Outline each blood parasite and name the species.
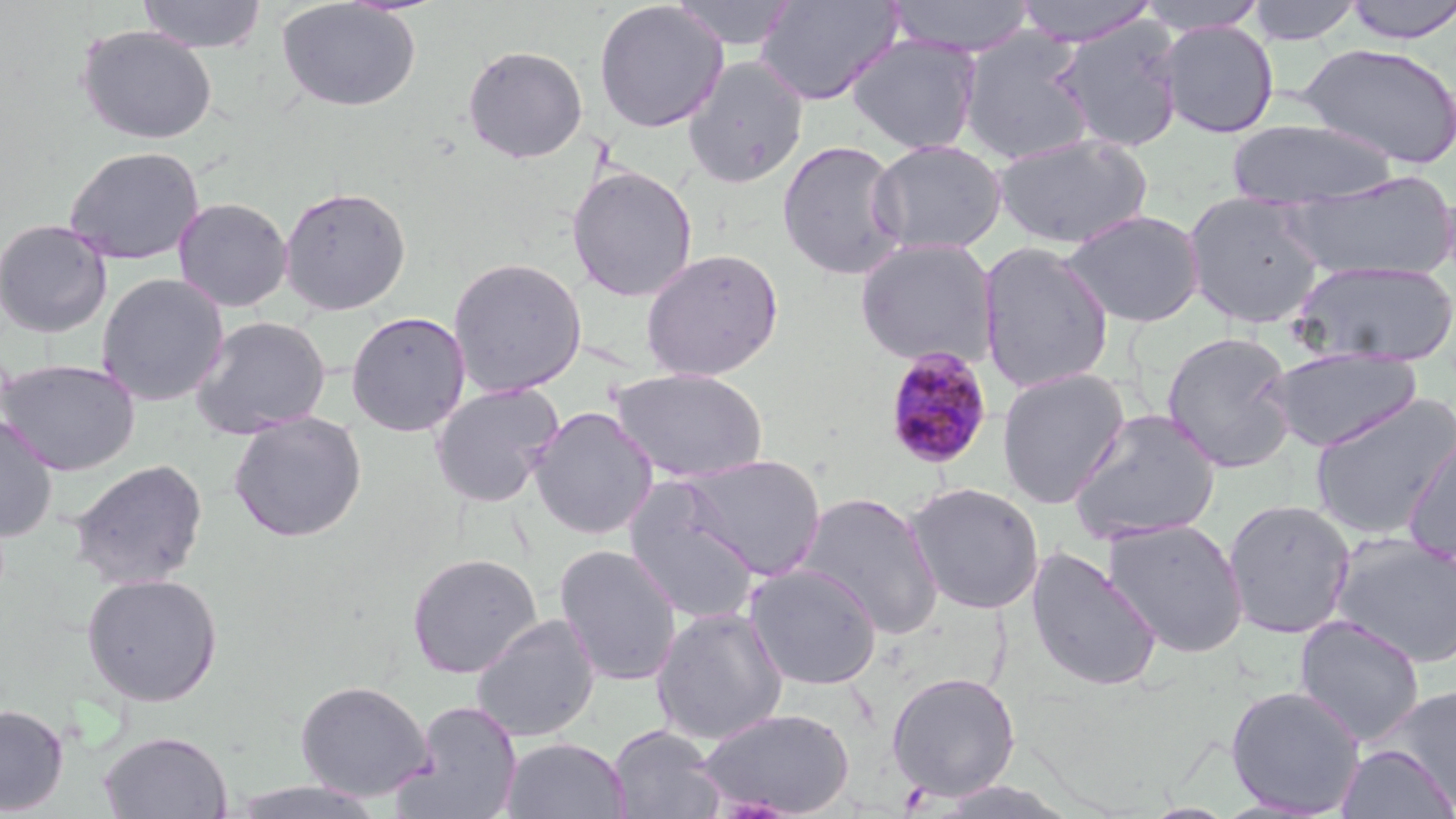
Approximate bounding boxes as (x1,y1)-(x2,y2) corner pairs in pixels.
Plasmodium malariae-infected red blood cells: (883,346)-(993,471).
No Plasmodium falciparum, Plasmodium ovale, Plasmodium vivax, Babesia divergens, or Trypanosoma brucei observed.

Summary:
  - Uninfected red blood cell locations: (136,0)-(267,54), (672,0)-(798,51), (886,0)-(1037,57), (1012,0)-(1159,46), (1342,0)-(1456,44), (593,1)-(728,133), (754,1)-(904,106), (1137,1)-(1269,35), (1244,1)-(1365,44), (276,2)-(422,113), (1051,17)-(1186,153), (1158,20)-(1279,139), (75,25)-(218,145), (958,30)-(1096,165), (845,34)-(984,155), (1298,41)-(1456,169), (462,44)-(589,163), (683,56)-(809,189), (1227,119)-(1397,208), (991,132)-(1154,250), (776,139)-(909,281), (869,139)-(1007,256), (63,145)-(205,265), (566,165)-(698,302), (1284,171)-(1455,282), (279,185)-(412,316), (1183,191)-(1328,329), (173,197)-(293,312), (1063,208)-(1206,327), (0,219)-(113,338), (855,238)-(999,369), (977,241)-(1114,394), (640,248)-(784,382), (447,256)-(587,398), (1291,259)-(1454,368), (95,273)-(229,407), (346,310)-(471,437), (189,315)-(331,439), (1161,331)-(1298,473), (1266,348)-(1422,451), (0,358)-(141,476), (608,366)-(769,483), (996,367)-(1131,509), (429,381)-(565,509), (1309,394)-(1455,541), (529,406)-(659,540), (1067,408)-(1222,545), (228,411)-(367,543), (0,414)-(59,543), (1401,426)-(1456,569), (681,453)-(826,581), (70,458)-(209,590), (622,476)-(763,624), (906,481)-(1045,615), (795,490)-(944,639), (1222,499)-(1357,639), (1101,517)-(1250,658), (1330,533)-(1456,669), (554,543)-(683,687), (1025,546)-(1163,692), (405,551)-(543,679), (744,563)-(883,691), (80,572)-(224,707), (650,606)-(789,746), (471,614)-(601,743), (1293,615)-(1426,747), (885,671)-(1021,801), (294,679)-(434,802), (1225,685)-(1366,817), (1373,685)-(1456,810), (396,701)-(523,819), (0,703)-(69,815), (697,706)-(855,817), (607,724)-(726,819), (98,730)-(233,818), (501,736)-(630,819), (1336,744)-(1455,819), (226,777)-(389,819), (933,778)-(1080,818)
  - Slide-level diagnosis: Plasmodium malariae
  - Stain: May-Grünwald-Giemsa
  - Image size: 1456×819 pixels
  - Field of view: single
  - Preparation: thin blood film
  - Modality: optical microscopy
  - Magnification: 1000x